Assess this cell for malaria.
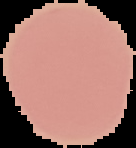

It is uninfected.

Summary:
  - Image type: cell region segmented out of the field of view; surrounding area masked to black
  - Image size: 136×148 pixels
  - Preparation: thin blood smear